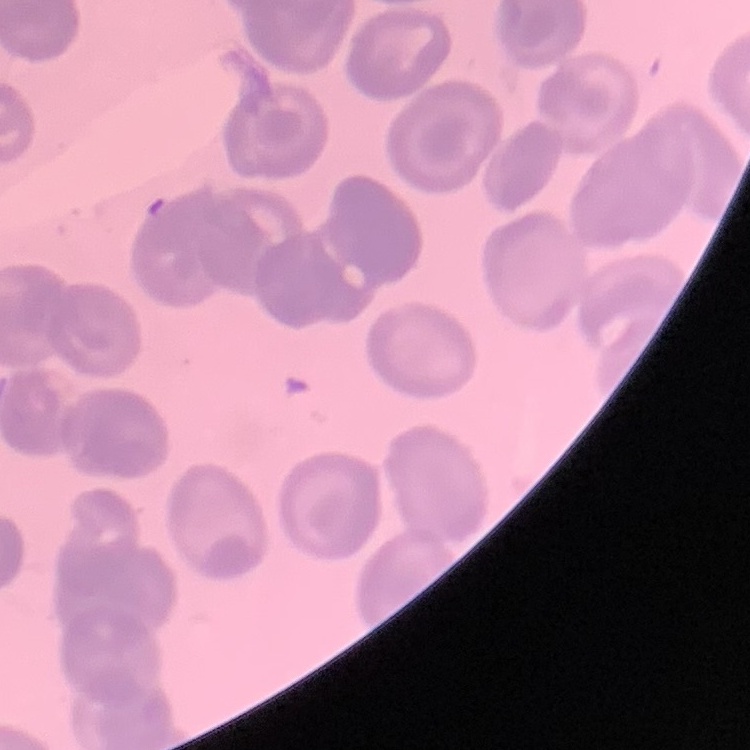
{
  "red_blood_cell_morphology": "no rouleaux formation",
  "image_type": "square crop of a larger photomicrograph",
  "preparation": "thin peripheral smear",
  "stain": "Field's or Giemsa"
}